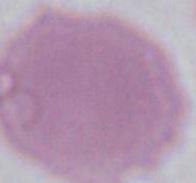
Summary:
  - Modality: micrograph
  - Identification: red blood cell
  - Magnification: 1000x